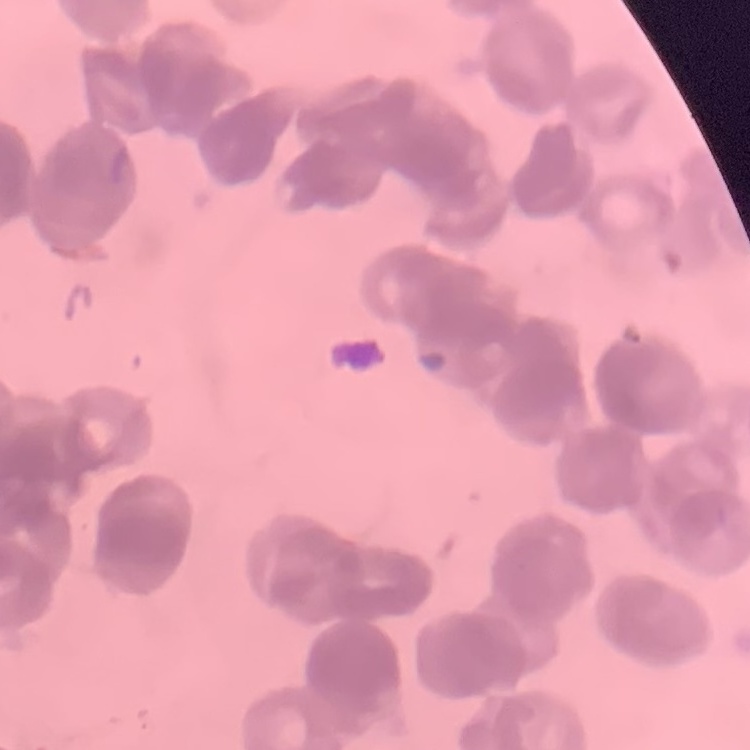

The erythrocytes show rouleaux formation. Square crop of a larger photomicrograph. Field's or Giemsa stain. Thin blood smear.